Locate and identify every blood parasite.
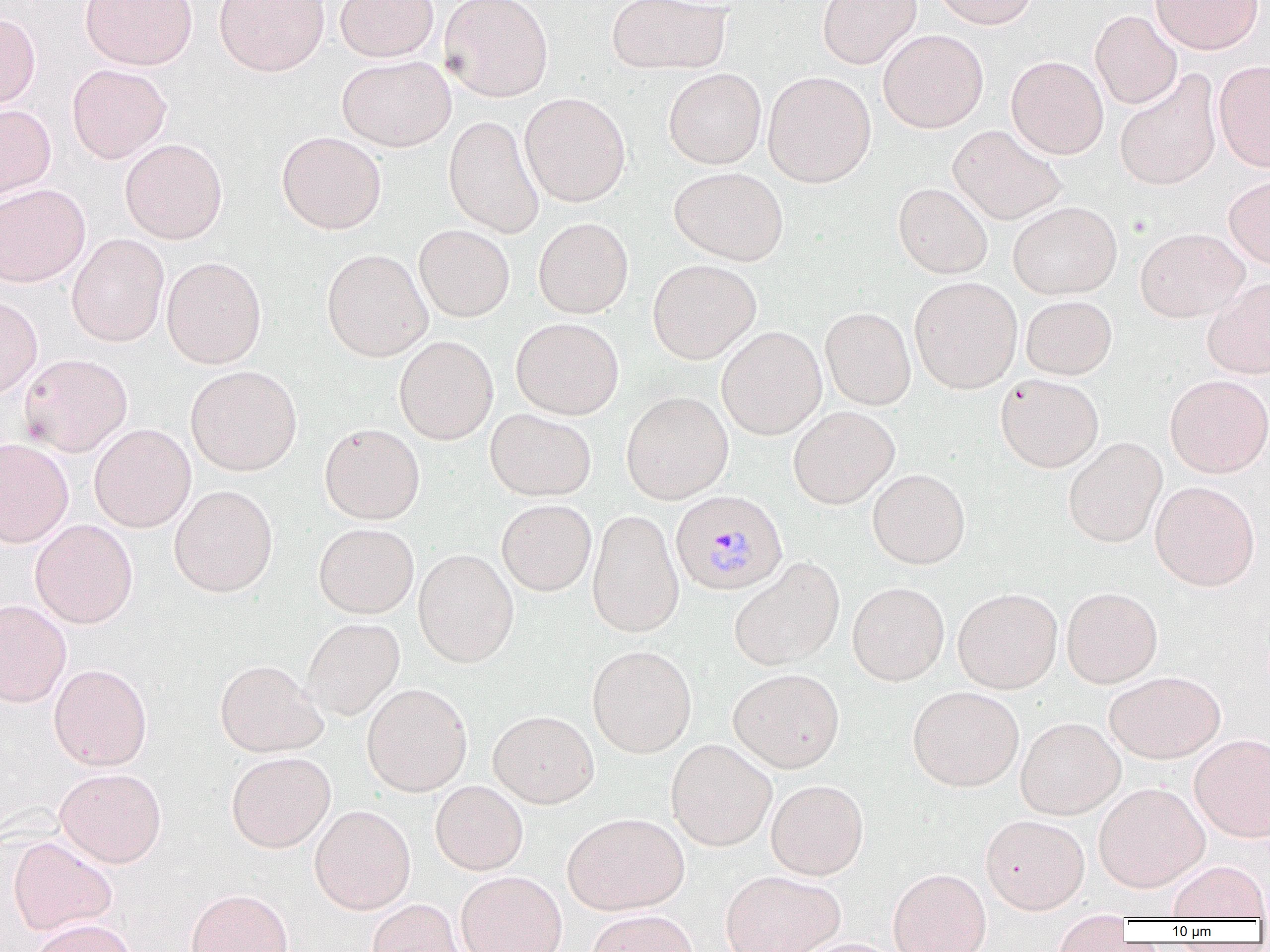
Approximate bounding boxes as named x1/y1/x2/y2 corners in pixels.
Plasmodium malariae-infected red blood cells: (x1=669, y1=490, x2=787, y2=596).
No Plasmodium falciparum, Plasmodium ovale, Plasmodium vivax, Babesia divergens, or Trypanosoma brucei observed.

Uninfected red blood cell locations: (x1=80, y1=0, x2=197, y2=70), (x1=214, y1=0, x2=329, y2=76), (x1=334, y1=0, x2=438, y2=61), (x1=439, y1=0, x2=554, y2=102), (x1=607, y1=0, x2=731, y2=75), (x1=817, y1=0, x2=921, y2=68), (x1=930, y1=0, x2=1038, y2=29), (x1=1150, y1=0, x2=1263, y2=54), (x1=1090, y1=10, x2=1182, y2=109), (x1=0, y1=12, x2=41, y2=109), (x1=878, y1=29, x2=988, y2=133), (x1=1006, y1=55, x2=1108, y2=159), (x1=337, y1=56, x2=455, y2=151), (x1=1213, y1=59, x2=1270, y2=171), (x1=67, y1=63, x2=171, y2=163), (x1=662, y1=68, x2=767, y2=169), (x1=763, y1=71, x2=876, y2=187), (x1=1114, y1=71, x2=1222, y2=190), (x1=519, y1=92, x2=630, y2=206), (x1=0, y1=104, x2=56, y2=202), (x1=443, y1=115, x2=544, y2=238), (x1=948, y1=124, x2=1067, y2=225), (x1=276, y1=131, x2=387, y2=234), (x1=120, y1=138, x2=227, y2=243), (x1=669, y1=167, x2=788, y2=265), (x1=1223, y1=175, x2=1270, y2=269), (x1=0, y1=183, x2=90, y2=287), (x1=893, y1=183, x2=993, y2=279), (x1=1008, y1=201, x2=1122, y2=299), (x1=533, y1=217, x2=634, y2=318), (x1=414, y1=224, x2=514, y2=322), (x1=1135, y1=227, x2=1248, y2=322), (x1=67, y1=234, x2=169, y2=347), (x1=321, y1=248, x2=432, y2=361), (x1=161, y1=256, x2=267, y2=369), (x1=647, y1=259, x2=761, y2=364), (x1=909, y1=276, x2=1023, y2=394), (x1=1203, y1=278, x2=1270, y2=379), (x1=0, y1=296, x2=43, y2=398), (x1=1020, y1=296, x2=1117, y2=380), (x1=820, y1=307, x2=916, y2=410), (x1=511, y1=317, x2=624, y2=419), (x1=716, y1=326, x2=827, y2=439), (x1=394, y1=335, x2=498, y2=444), (x1=19, y1=353, x2=133, y2=456), (x1=185, y1=365, x2=302, y2=476), (x1=996, y1=373, x2=1104, y2=473), (x1=1164, y1=375, x2=1270, y2=478), (x1=621, y1=391, x2=734, y2=504), (x1=788, y1=406, x2=899, y2=509), (x1=485, y1=408, x2=596, y2=501), (x1=319, y1=423, x2=425, y2=524), (x1=89, y1=424, x2=196, y2=532), (x1=1063, y1=437, x2=1167, y2=547), (x1=0, y1=438, x2=74, y2=547), (x1=867, y1=468, x2=970, y2=569), (x1=1150, y1=481, x2=1260, y2=591), (x1=169, y1=485, x2=278, y2=597), (x1=497, y1=499, x2=596, y2=596), (x1=587, y1=509, x2=684, y2=638), (x1=30, y1=519, x2=138, y2=628), (x1=313, y1=522, x2=419, y2=618), (x1=413, y1=548, x2=519, y2=667), (x1=729, y1=557, x2=845, y2=671), (x1=847, y1=582, x2=950, y2=686), (x1=953, y1=587, x2=1062, y2=693), (x1=1061, y1=587, x2=1162, y2=688), (x1=0, y1=600, x2=71, y2=707), (x1=303, y1=617, x2=405, y2=721), (x1=587, y1=644, x2=697, y2=758), (x1=214, y1=659, x2=327, y2=757), (x1=49, y1=663, x2=152, y2=770), (x1=728, y1=668, x2=845, y2=773), (x1=1104, y1=670, x2=1226, y2=762), (x1=361, y1=683, x2=473, y2=796), (x1=907, y1=686, x2=1024, y2=792), (x1=488, y1=709, x2=599, y2=808), (x1=1015, y1=716, x2=1125, y2=819), (x1=1190, y1=734, x2=1270, y2=841), (x1=665, y1=739, x2=777, y2=851), (x1=226, y1=751, x2=336, y2=852), (x1=54, y1=767, x2=167, y2=867), (x1=766, y1=779, x2=869, y2=880), (x1=430, y1=780, x2=528, y2=875), (x1=1093, y1=782, x2=1209, y2=892), (x1=309, y1=804, x2=416, y2=914), (x1=562, y1=812, x2=690, y2=915), (x1=980, y1=814, x2=1090, y2=913), (x1=8, y1=836, x2=117, y2=935), (x1=1167, y1=859, x2=1269, y2=921), (x1=888, y1=867, x2=991, y2=952), (x1=720, y1=869, x2=845, y2=952), (x1=456, y1=871, x2=567, y2=952), (x1=186, y1=888, x2=293, y2=952), (x1=366, y1=898, x2=467, y2=952), (x1=586, y1=909, x2=699, y2=952), (x1=1052, y1=913, x2=1134, y2=952), (x1=29, y1=918, x2=139, y2=952), (x1=794, y1=937, x2=904, y2=952). Slide-level diagnosis: Plasmodium malariae. Captured at 1000x magnification. Light microscopy. Single field of view. Image is 1270×952 pixels. Thin blood film.